Identify the parasite.
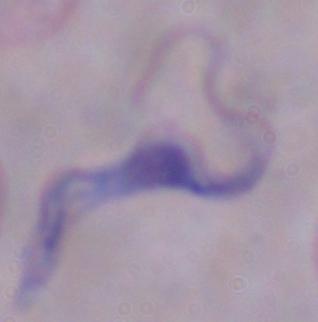

This is a trypanosome.

modality = micrograph
magnification = 1000x